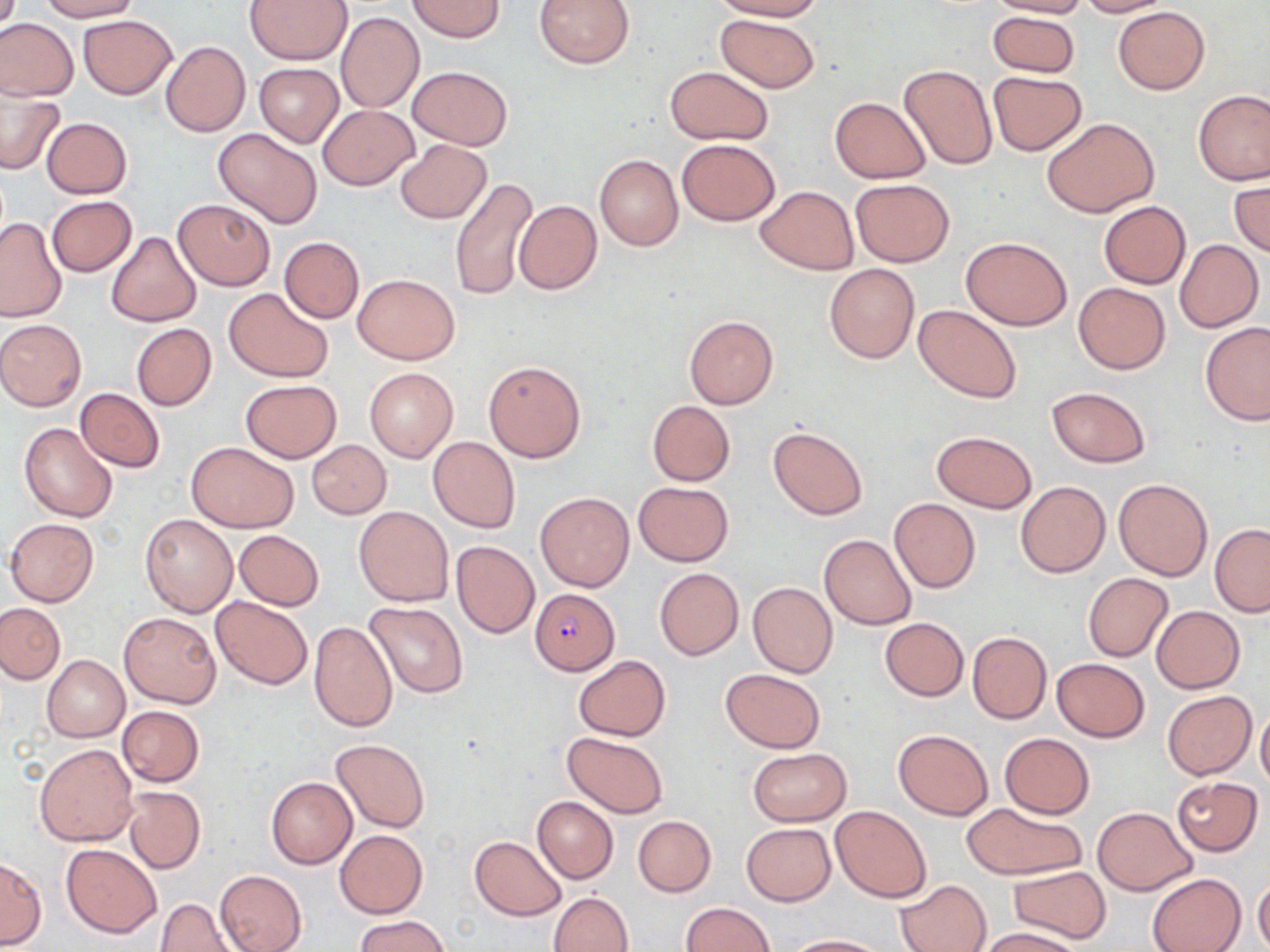
slide_level_diagnosis: Plasmodium falciparum
modality: optical microscopy
preparation: thin blood film
image_size: 1270×952 pixels
field_of_view: single
magnification: 1000x
stain: May-Grünwald-Giemsa
uninfected_red_blood_cell_locations: 'approximate bounding boxes as [x1, y1, x2, y2] in pixels: [37, 0, 141, 22], [244, 0, 352, 65], [407, 0, 506, 41], [534, 0, 636, 69], [711, 0, 825, 21], [988, 0, 1089, 18], [1074, 0, 1171, 17], [1113, 6, 1209, 94], [336, 10, 424, 113], [988, 11, 1081, 80], [714, 13, 821, 92], [78, 15, 178, 99], [0, 19, 78, 100], [160, 41, 251, 138], [254, 64, 343, 148], [898, 64, 996, 170], [407, 65, 512, 150], [664, 66, 775, 146], [988, 70, 1086, 155], [0, 89, 64, 175], [1192, 89, 1270, 185], [830, 97, 930, 182], [317, 104, 419, 190], [41, 117, 132, 198], [1043, 117, 1159, 217], [213, 128, 321, 228], [394, 139, 491, 223], [676, 139, 780, 226], [594, 154, 683, 250], [449, 176, 538, 301], [1229, 178, 1269, 258], [850, 179, 954, 265], [756, 185, 857, 275], [47, 196, 137, 276], [173, 197, 275, 290], [514, 199, 602, 294], [1099, 201, 1191, 288], [0, 217, 67, 322], [105, 231, 201, 328], [278, 236, 364, 323], [961, 237, 1072, 331], [1174, 240, 1264, 331], [824, 264, 919, 362], [353, 274, 460, 365], [1072, 281, 1170, 374], [224, 289, 334, 384], [914, 305, 1019, 403], [684, 315, 779, 408], [0, 319, 87, 411], [1199, 322, 1269, 426], [131, 323, 217, 410], [483, 361, 586, 462], [364, 367, 458, 463], [240, 379, 342, 462], [1047, 386, 1151, 468], [75, 388, 165, 473], [646, 400, 735, 485], [18, 421, 118, 523], [768, 427, 868, 520], [931, 431, 1038, 512], [428, 436, 520, 533], [307, 440, 391, 519], [187, 442, 299, 533], [1113, 478, 1213, 579], [1015, 480, 1111, 577], [634, 482, 733, 566], [537, 492, 634, 591], [889, 498, 980, 593], [353, 506, 452, 607], [139, 514, 238, 618], [4, 517, 99, 606], [1210, 523, 1270, 616], [233, 529, 325, 610], [819, 534, 916, 629], [451, 540, 539, 638], [654, 567, 743, 659], [1083, 573, 1173, 661], [747, 582, 838, 678], [211, 595, 313, 690], [364, 601, 467, 699], [0, 602, 65, 684], [1150, 605, 1245, 693], [118, 612, 220, 708], [880, 618, 968, 701], [308, 621, 398, 733], [966, 631, 1052, 724], [42, 656, 129, 743], [573, 656, 671, 740], [1052, 659, 1148, 741], [720, 668, 826, 751], [1163, 689, 1256, 780], [118, 705, 203, 787], [1256, 706, 1270, 790], [893, 728, 994, 819], [562, 731, 668, 818], [1000, 733, 1093, 817], [331, 739, 429, 832], [36, 743, 139, 848], [746, 747, 852, 826], [266, 776, 357, 869], [1172, 777, 1263, 856], [123, 786, 205, 873], [533, 796, 618, 883], [960, 802, 1085, 880], [831, 806, 931, 902], [1092, 806, 1197, 896], [632, 815, 716, 896], [741, 822, 836, 905], [335, 831, 427, 917], [469, 835, 566, 920], [62, 844, 162, 935], [0, 858, 46, 947], [1010, 865, 1111, 945], [215, 869, 306, 952], [1147, 873, 1246, 952], [1253, 876, 1270, 950], [350, 877, 438, 952], [896, 879, 992, 952], [549, 891, 633, 952], [155, 897, 239, 951], [679, 902, 774, 952], [355, 914, 451, 952], [975, 928, 1081, 952], [782, 935, 885, 952]'
plasmodium_falciparum_infected_red_blood_cell_locations: 'approximate bounding boxes as [x1, y1, x2, y2] in pixels: [529, 588, 620, 675]'